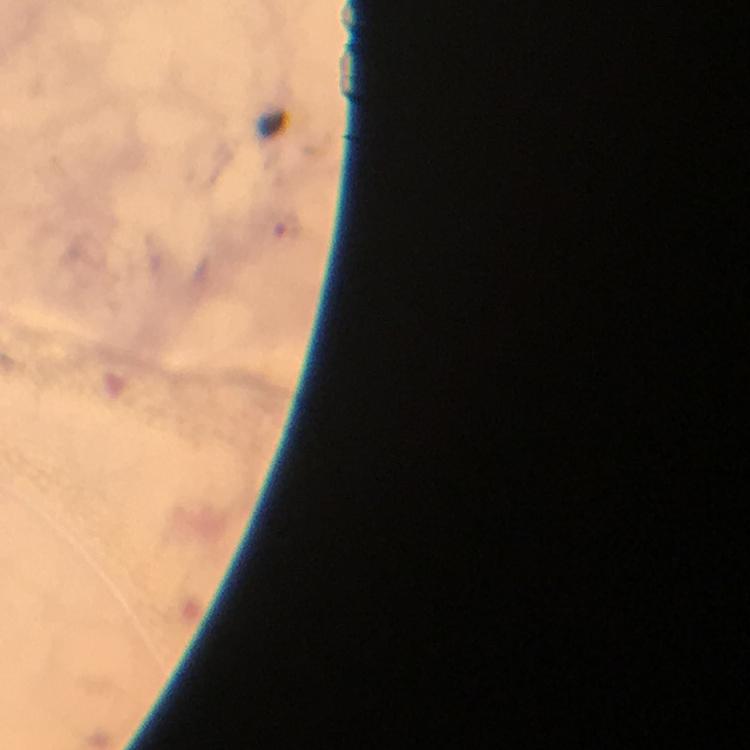

Approximate centers as {x, y} in pixels.
Summary:
  - Malaria parasite locations: {291, 227}
  - Image size: 750×750 pixels
  - Magnification: 100x
  - Preparation: thick blood smear
  - Stain: Giemsa
  - Cropped from: one field of view
  - Context: from a diagnostic examination for malaria
  - Capture: smartphone photograph through a microscope
  - Immersion oil: applied